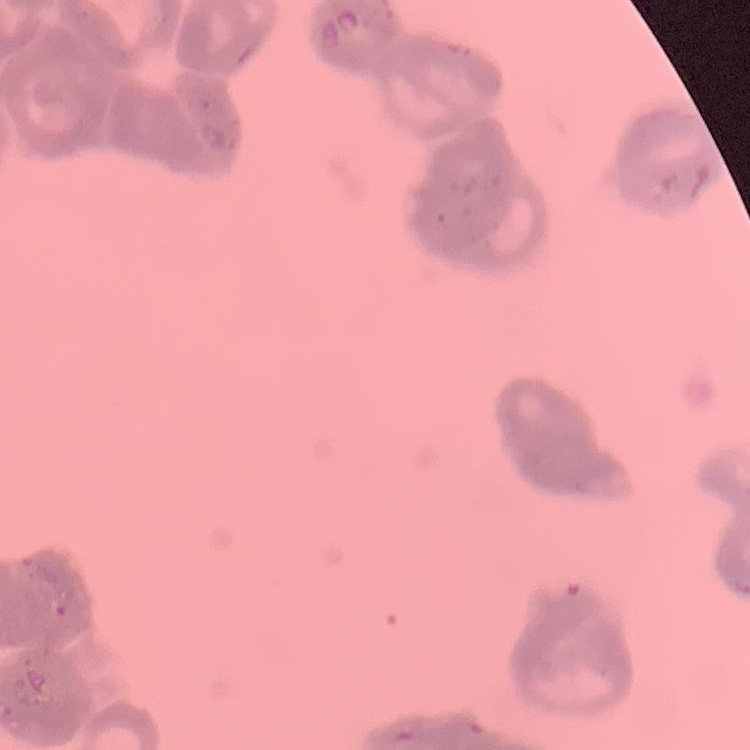
The erythrocytes show rouleaux formation. One tile cut from a larger photomicrograph. Field's or Giemsa stain. Thin peripheral smear.